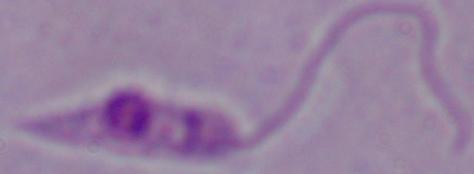 A Leishmania parasite is seen. 1000x magnification. Photomicrograph.